Classify this cell by malaria status.
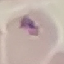

Uninfected.

Giemsa-stained preparation. Cell patch, automatically extracted from a larger field of view and resized to 64 × 64 pixels. Thin blood film. Acquired by smartphone through the microscope eyepiece.